Identify the parasite.
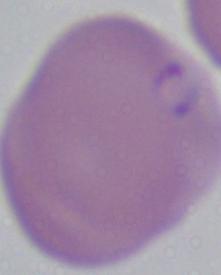
This is Babesia.

1000x magnification. Photomicrograph.